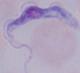

Summary:
  - Identification: trypanosome
  - Modality: photomicrograph
  - Magnification: 1000x